Classify this cell by malaria status.
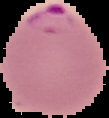

Parasitized.

image size = 109×118 pixels
preparation = thin blood film
image type = cell region segmented out of the field of view; surrounding area masked to black